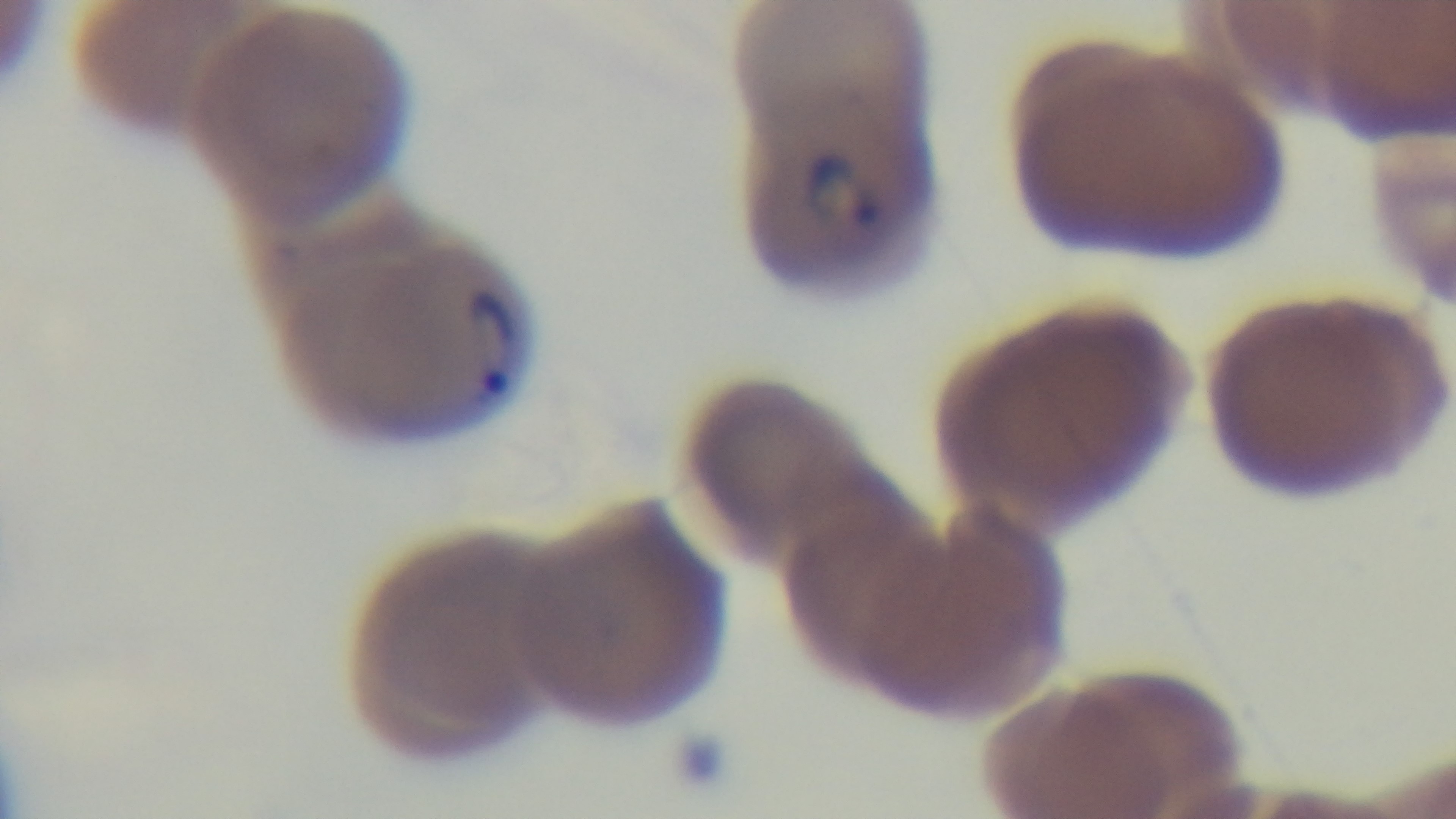

field of view = one from the slide
objective = 100x oil immersion
malaria status = positive
capture = mounted 4K digital camera
preparation = thin
stain = Giemsa
modality = light microscopy